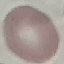

Malaria status: uninfected. Thin blood film. Automatically extracted cell patch, resized to 64 × 64 pixels. Giemsa-stained preparation. Acquired by smartphone through the microscope eyepiece.